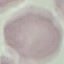
{
  "result": "negative for malaria parasites",
  "capture": "smartphone camera at the microscope eyepiece",
  "preparation": "thin blood smear",
  "stain": "Giemsa",
  "image_type": "automatically extracted cell patch, resized to 64 × 64 pixels"
}